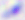
Summary:
  - Identification: Toxoplasma gondii
  - Modality: micrograph
  - Magnification: 400x